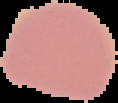 From a thin blood film. Result: no Plasmodium parasites seen. Image is 118×103 pixels. Segmented cell region on a black background.